Report the malaria status of this cell.
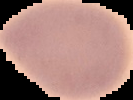
Uninfected.

Segmented cell region on a black background. From a thin blood smear. Image is 133×100 pixels.